Give the position of every Plasmodium parasite visible.
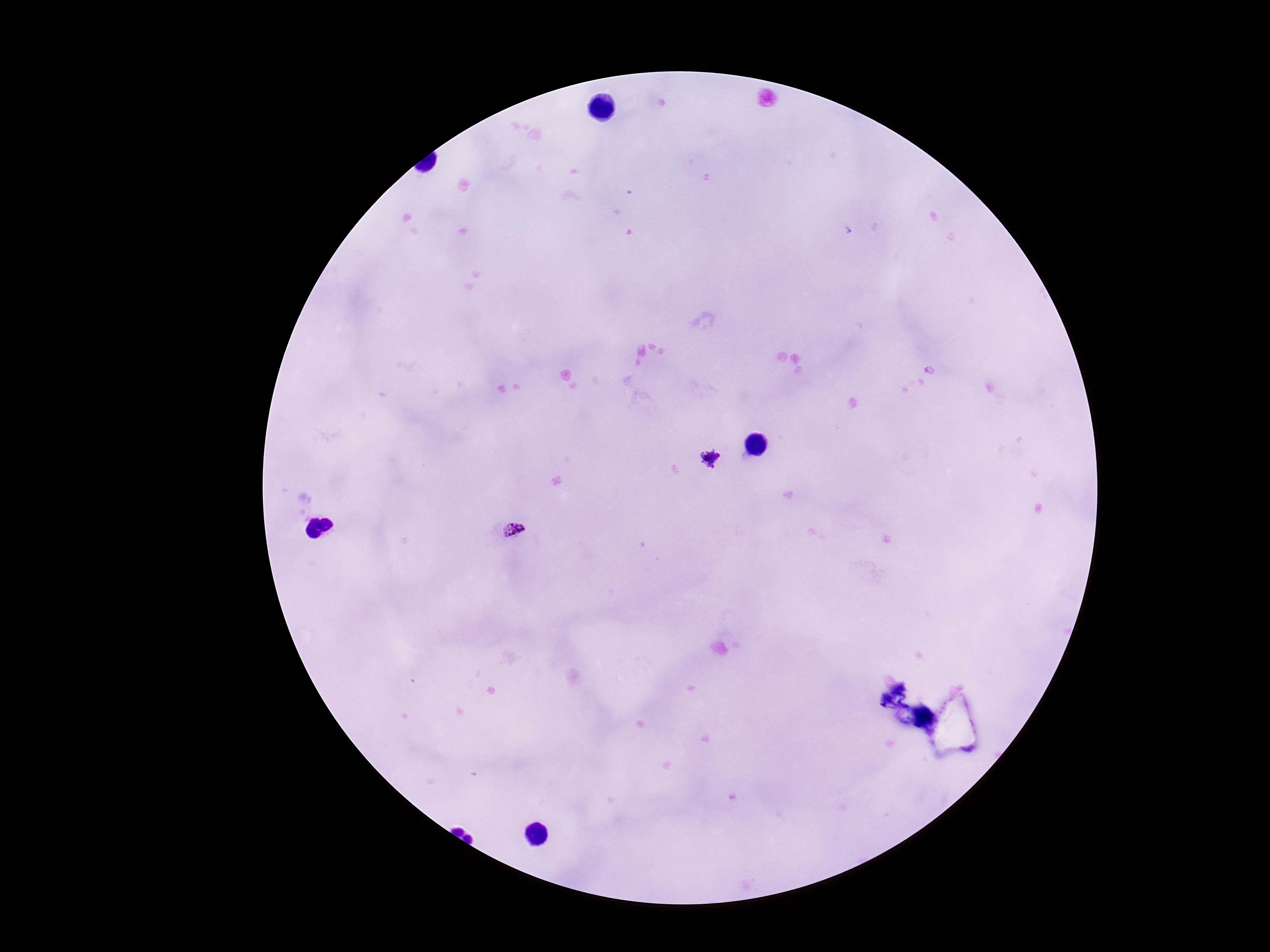

Approximate object centers, in pixels from the top-left corner.
Plasmodium parasites: (x=707, y=458), (x=514, y=530).

{
  "patient_malaria_status": "infected",
  "preparation": "thick blood film",
  "stain": "Giemsa",
  "image_size": "1270×952 pixels",
  "magnification": "100x",
  "field_of_view": "one from this slide",
  "capture": "smartphone camera through the microscope eyepiece"
}